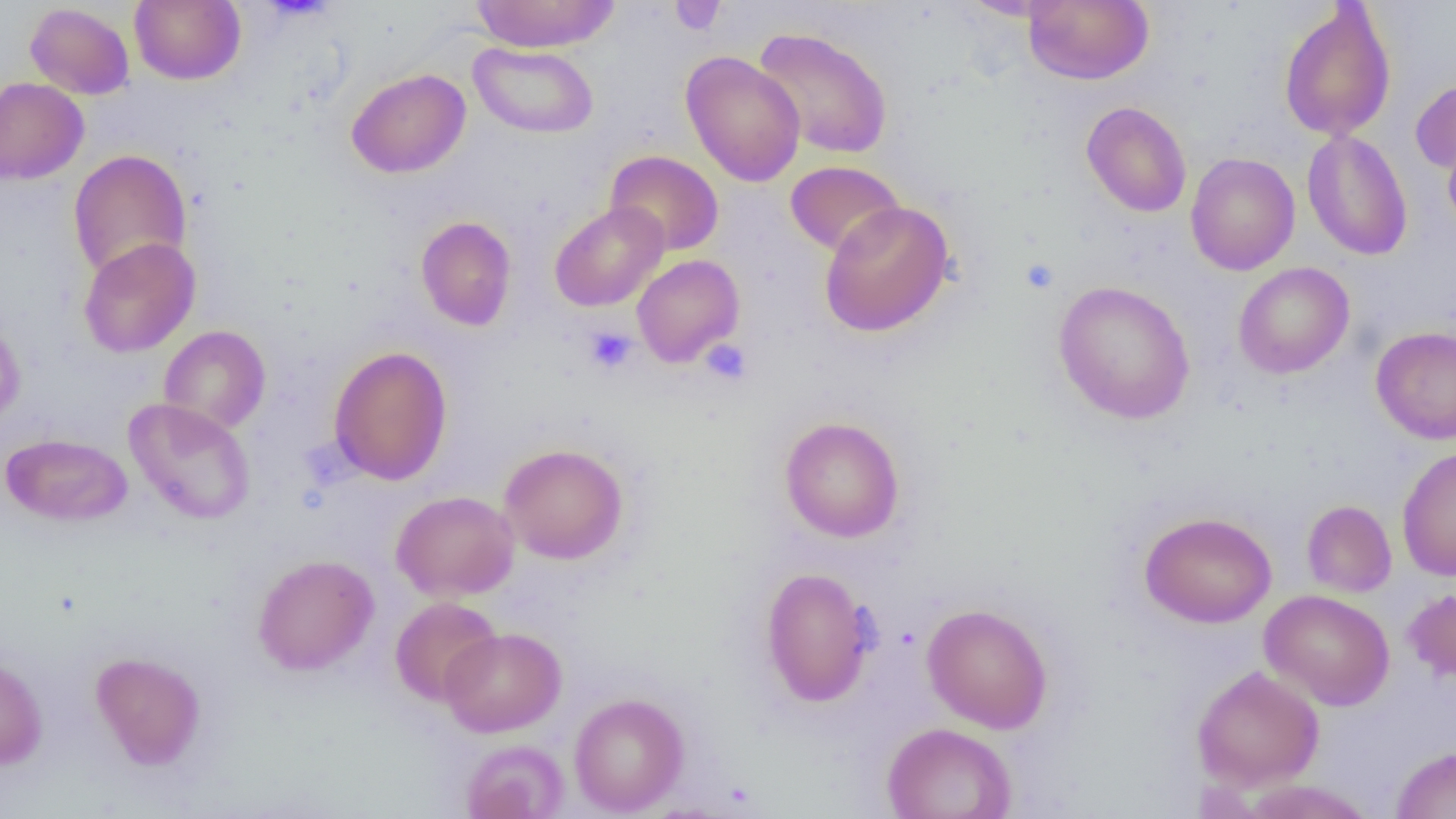
slide-level diagnosis = no evidence of blood parasites
magnification = 1000x
platelet locations (subset) = approximate bounding boxes as (x1,y1)-(x2,y2) corner pairs in pixels: (1021,258)-(1059,294), (583,326)-(638,375), (700,340)-(752,386)
uninfected red blood cell locations (subset) = approximate bounding boxes as (x1,y1)-(x2,y2) corner pairs in pixels: (130,0)-(245,85), (469,0)-(621,52), (957,0)-(1070,21), (1022,0)-(1154,85), (1278,2)-(1397,142), (25,3)-(134,99), (752,25)-(893,159), (468,42)-(599,139), (680,51)-(806,187), (346,68)-(471,178), (1410,75)-(1456,176), (0,76)-(89,185), (1081,101)-(1192,217), (1443,129)-(1456,239), (1301,130)-(1413,261), (68,149)-(192,282), (604,150)-(724,256), (1185,152)-(1300,276), (785,160)-(905,257), (819,200)-(955,338), (549,201)-(669,311), (415,216)-(517,331), (78,237)-(200,358), (631,254)-(745,367), (1233,262)-(1355,379), (1053,280)-(1196,424), (0,312)-(26,428), (158,325)-(271,434), (1370,326)-(1456,444), (328,346)-(453,485), (124,398)-(256,525), (779,416)-(906,542), (1,433)-(133,527), (499,443)-(628,564), (1397,446)-(1456,581), (391,490)-(519,601), (1302,500)-(1397,597), (1140,511)-(1277,628), (252,553)-(379,675), (760,567)-(876,707), (1402,585)-(1456,685), (1259,589)-(1395,711), (390,596)-(502,707), (921,603)-(1054,733), (440,627)-(566,737), (90,651)-(207,770), (0,653)-(48,770), (1191,665)-(1325,791), (569,692)-(689,815), (881,722)-(1017,819), (460,739)-(569,819), (1390,745)-(1456,819), (1238,779)-(1379,818)
modality = optical microscopy
preparation = thin blood smear
image size = 1456×819 pixels
field of view = one of a larger specimen